Locate Plasmodium parasites and leukocytes.
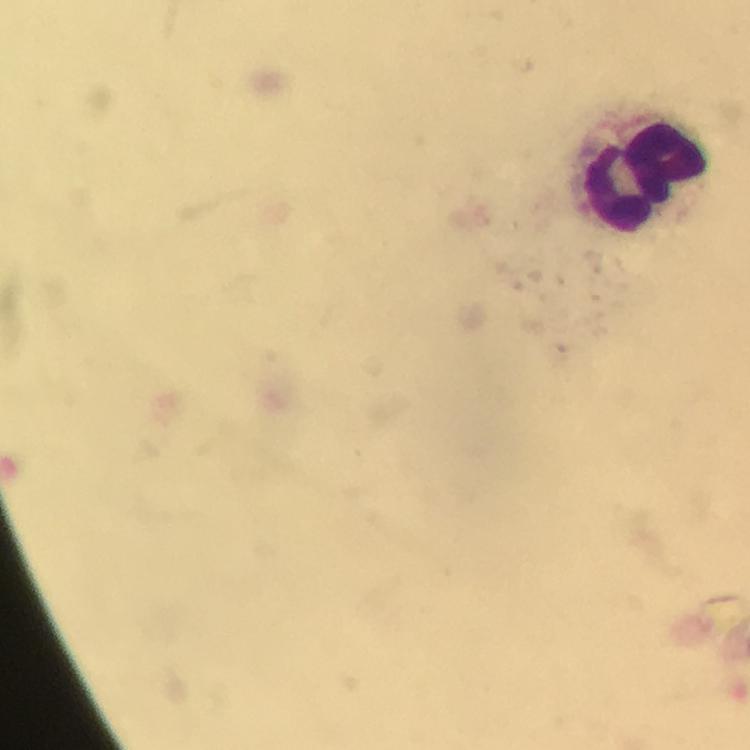
No Plasmodium parasites detected.
Approximate centers as [x, y] in pixels.
Leukocytes: [645, 177].

Summary:
  - Context: from a malaria diagnostic workup
  - Immersion oil: used
  - Capture: smartphone mounted on the microscope
  - Stain: Giemsa
  - Cropped from: a single field of view
  - Image size: 750×750 pixels
  - Magnification: 100x
  - Preparation: thick blood film